Give the position of every Plasmodium parasite.
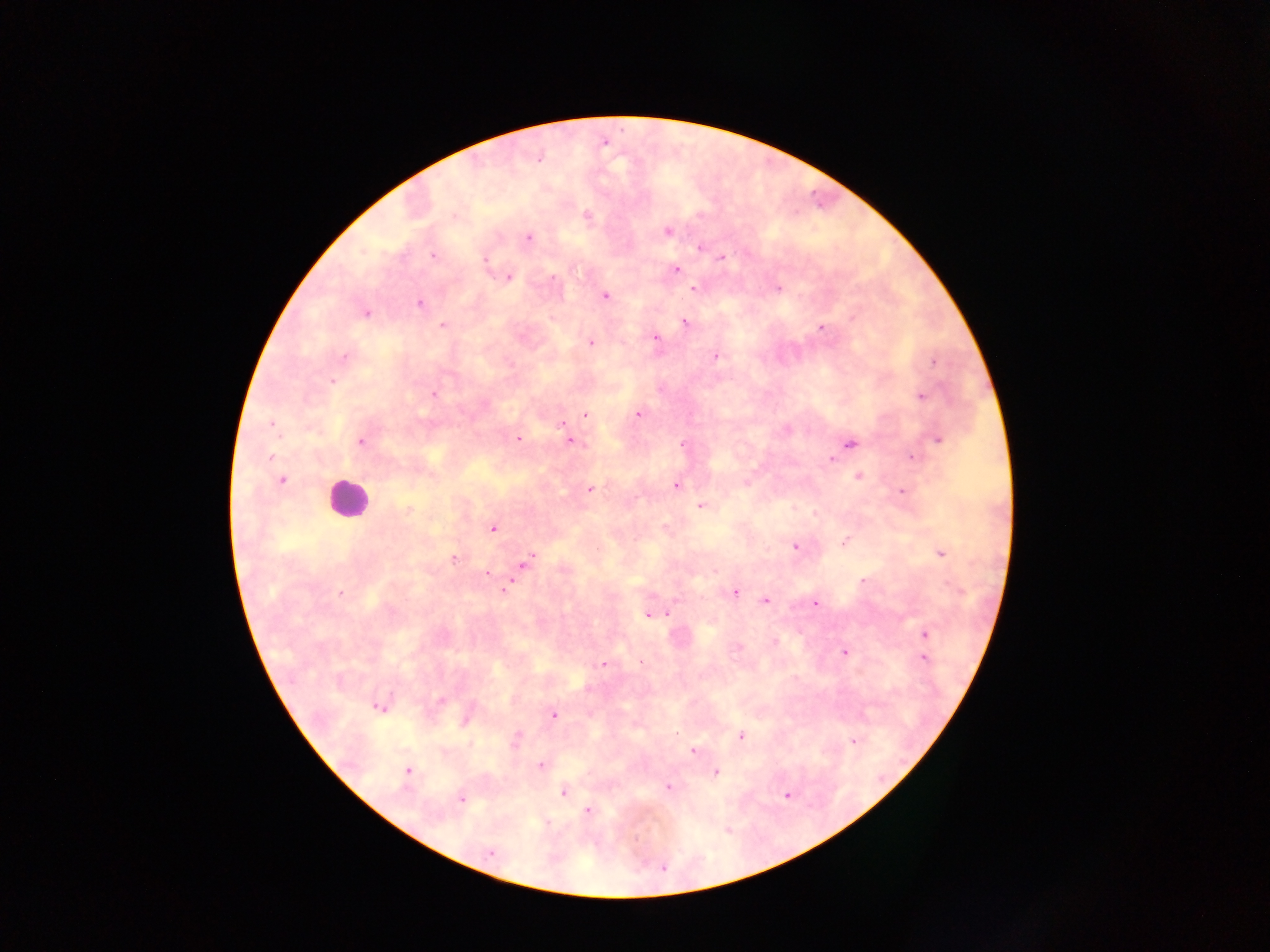
Approximate centers as x y in pixels.
Plasmodium parasites: 453 215; 587 215; 668 231; 529 238; 699 248; 433 255; 722 257; 485 261; 677 270; 509 277; 554 278; 778 287; 694 288; 606 296; 420 303; 365 313; 853 318; 685 323; 442 325; 820 327; 655 338; 590 342; 344 356; 716 357; 934 361; 333 381; 434 395; 921 396; 638 414; 586 415; 561 423; 271 424; 517 438; 938 440; 570 441; 360 442; 682 444; 850 444; 270 457; 912 457; 830 459; 858 476; 282 480; 746 484; 676 485; 589 490; 902 492; 701 506; 408 509; 494 529; 845 541; 795 547; 940 553; 453 558; 526 562; 486 572; 863 580; 505 589; 734 593; 341 594; 766 601; 816 603; 667 614; 647 616; 924 634; 774 643; 844 652; 925 659; 603 664; 442 700; 378 707; 554 715; 467 720; 741 736; 853 741; 516 743; 693 751; 541 765; 407 771; 716 772; 669 787; 563 793; 786 795; 462 800; 588 811; 490 852; 663 868.

country = Ghana
field of view = single
image size = 1270×952 pixels
preparation = thick blood smear
capture = mobile-phone photograph through a microscope
leukocyte locations = approximate centers as x y in pixels: 346 498